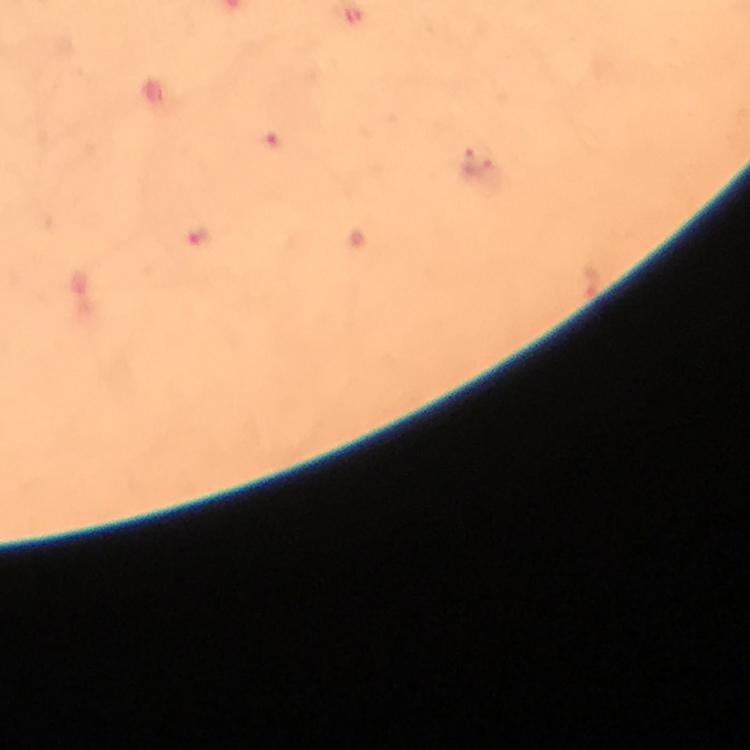
{
  "context": "from a malaria diagnostic workup",
  "capture": "smartphone mounted on the microscope",
  "stain": "Giemsa",
  "preparation": "thick smear",
  "magnification": "100x",
  "immersion_oil": "applied",
  "cropped_from": "a single field of view",
  "image_size": "750×750 pixels",
  "malaria_parasite_locations": "approximate centers as [x, y] in pixels: [278, 141], [201, 235]"
}